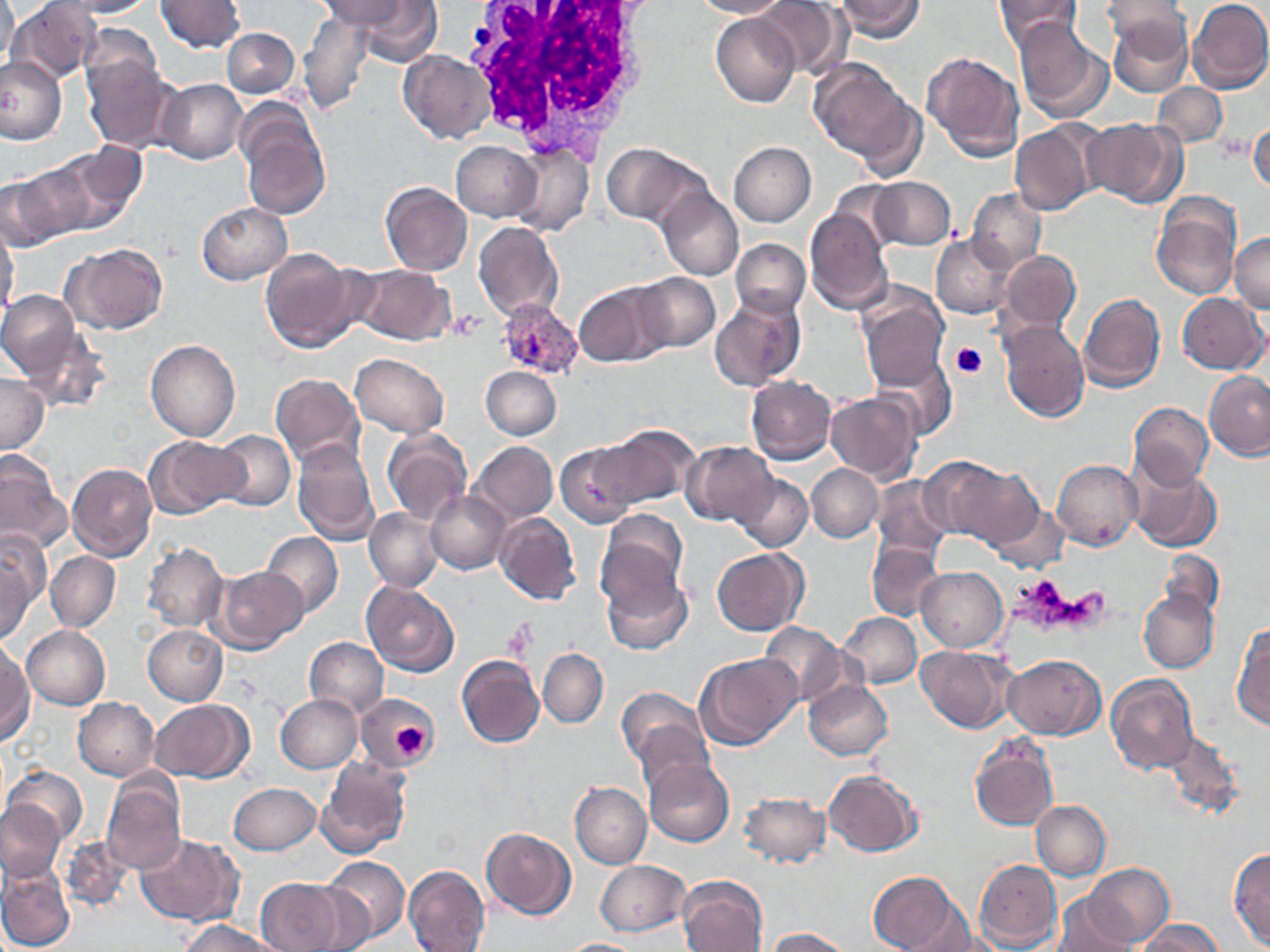

Approximate bounding boxes as named x1/y1/x2/y2 corners in pixels. White blood cell locations: (x1=461, y1=0, x2=660, y2=165). Platelet locations: (x1=448, y1=311, x2=484, y2=341), (x1=952, y1=342, x2=988, y2=379), (x1=504, y1=622, x2=538, y2=661), (x1=393, y1=720, x2=428, y2=758). Uninfected red blood cell locations: (x1=1, y1=0, x2=18, y2=74), (x1=7, y1=0, x2=103, y2=84), (x1=57, y1=0, x2=154, y2=18), (x1=155, y1=0, x2=244, y2=53), (x1=321, y1=0, x2=420, y2=36), (x1=691, y1=0, x2=788, y2=19), (x1=756, y1=0, x2=846, y2=79), (x1=834, y1=0, x2=925, y2=41), (x1=993, y1=0, x2=1083, y2=47), (x1=1186, y1=0, x2=1270, y2=93), (x1=352, y1=1, x2=443, y2=65), (x1=1102, y1=1, x2=1192, y2=54), (x1=297, y1=9, x2=374, y2=117), (x1=711, y1=12, x2=800, y2=107), (x1=1107, y1=15, x2=1192, y2=98), (x1=1012, y1=18, x2=1111, y2=121), (x1=225, y1=21, x2=365, y2=109), (x1=78, y1=23, x2=163, y2=101), (x1=222, y1=27, x2=298, y2=98), (x1=398, y1=49, x2=496, y2=144), (x1=922, y1=51, x2=1024, y2=161), (x1=0, y1=55, x2=66, y2=145), (x1=81, y1=56, x2=175, y2=153), (x1=809, y1=59, x2=914, y2=161), (x1=158, y1=79, x2=247, y2=165), (x1=1153, y1=82, x2=1227, y2=148), (x1=856, y1=99, x2=927, y2=184), (x1=237, y1=105, x2=330, y2=220), (x1=1083, y1=116, x2=1189, y2=208), (x1=1248, y1=116, x2=1270, y2=197), (x1=1009, y1=121, x2=1100, y2=216), (x1=452, y1=141, x2=542, y2=222), (x1=728, y1=142, x2=816, y2=226), (x1=600, y1=143, x2=709, y2=228), (x1=507, y1=144, x2=593, y2=238), (x1=46, y1=146, x2=143, y2=232), (x1=0, y1=172, x2=73, y2=250), (x1=868, y1=177, x2=956, y2=251), (x1=379, y1=182, x2=472, y2=275), (x1=657, y1=188, x2=743, y2=280), (x1=967, y1=188, x2=1046, y2=273), (x1=1151, y1=194, x2=1241, y2=301), (x1=197, y1=202, x2=292, y2=284), (x1=804, y1=207, x2=894, y2=314), (x1=0, y1=219, x2=20, y2=322), (x1=473, y1=223, x2=562, y2=322), (x1=931, y1=232, x2=1016, y2=318), (x1=1230, y1=234, x2=1270, y2=312), (x1=731, y1=239, x2=810, y2=318), (x1=63, y1=241, x2=169, y2=335), (x1=259, y1=247, x2=361, y2=352), (x1=996, y1=250, x2=1081, y2=336), (x1=353, y1=264, x2=455, y2=345), (x1=631, y1=273, x2=720, y2=353), (x1=574, y1=282, x2=667, y2=367), (x1=856, y1=287, x2=949, y2=388), (x1=0, y1=290, x2=80, y2=380), (x1=1077, y1=291, x2=1166, y2=394), (x1=1178, y1=292, x2=1268, y2=375), (x1=709, y1=296, x2=803, y2=392), (x1=997, y1=319, x2=1088, y2=423), (x1=20, y1=328, x2=112, y2=414), (x1=146, y1=340, x2=240, y2=441), (x1=869, y1=353, x2=958, y2=441), (x1=350, y1=354, x2=449, y2=438), (x1=481, y1=367, x2=561, y2=439), (x1=1204, y1=371, x2=1270, y2=461), (x1=0, y1=373, x2=49, y2=455), (x1=270, y1=373, x2=366, y2=469), (x1=745, y1=376, x2=836, y2=464), (x1=824, y1=392, x2=921, y2=484), (x1=1128, y1=403, x2=1213, y2=490), (x1=597, y1=425, x2=700, y2=510), (x1=381, y1=428, x2=473, y2=526), (x1=213, y1=430, x2=295, y2=512), (x1=143, y1=435, x2=249, y2=518), (x1=292, y1=440, x2=380, y2=546), (x1=469, y1=441, x2=558, y2=524), (x1=555, y1=441, x2=641, y2=526), (x1=680, y1=441, x2=778, y2=527), (x1=0, y1=454, x2=67, y2=555), (x1=922, y1=456, x2=1030, y2=546), (x1=1052, y1=459, x2=1143, y2=551), (x1=1126, y1=459, x2=1222, y2=552), (x1=67, y1=462, x2=159, y2=561), (x1=806, y1=464, x2=883, y2=542), (x1=733, y1=473, x2=812, y2=552), (x1=871, y1=476, x2=953, y2=560), (x1=426, y1=492, x2=511, y2=574), (x1=988, y1=503, x2=1068, y2=575), (x1=364, y1=508, x2=443, y2=592), (x1=494, y1=512, x2=582, y2=606), (x1=597, y1=512, x2=688, y2=615), (x1=0, y1=531, x2=49, y2=616), (x1=262, y1=532, x2=342, y2=617), (x1=866, y1=540, x2=944, y2=623), (x1=143, y1=542, x2=227, y2=632), (x1=711, y1=548, x2=807, y2=635), (x1=1156, y1=550, x2=1224, y2=624), (x1=0, y1=551, x2=34, y2=645), (x1=45, y1=551, x2=120, y2=631), (x1=213, y1=565, x2=309, y2=653), (x1=915, y1=566, x2=1007, y2=652), (x1=602, y1=570, x2=692, y2=655), (x1=360, y1=582, x2=460, y2=677), (x1=1139, y1=590, x2=1218, y2=674), (x1=838, y1=612, x2=922, y2=688), (x1=1231, y1=621, x2=1270, y2=731), (x1=758, y1=623, x2=850, y2=707), (x1=144, y1=624, x2=228, y2=704), (x1=22, y1=625, x2=111, y2=710), (x1=304, y1=638, x2=388, y2=717), (x1=916, y1=646, x2=1014, y2=732), (x1=538, y1=648, x2=609, y2=728), (x1=0, y1=650, x2=32, y2=747), (x1=695, y1=652, x2=802, y2=749), (x1=1003, y1=654, x2=1105, y2=739), (x1=456, y1=656, x2=544, y2=750), (x1=1106, y1=674, x2=1196, y2=772), (x1=803, y1=681, x2=893, y2=761), (x1=617, y1=688, x2=709, y2=769), (x1=356, y1=691, x2=438, y2=769), (x1=275, y1=694, x2=363, y2=773), (x1=72, y1=697, x2=160, y2=781), (x1=149, y1=700, x2=253, y2=781), (x1=634, y1=720, x2=715, y2=799), (x1=1161, y1=731, x2=1245, y2=819), (x1=969, y1=738, x2=1057, y2=832), (x1=317, y1=757, x2=411, y2=858), (x1=643, y1=757, x2=733, y2=847), (x1=4, y1=765, x2=87, y2=847), (x1=823, y1=770, x2=921, y2=856), (x1=102, y1=773, x2=186, y2=874), (x1=570, y1=782, x2=652, y2=868), (x1=228, y1=783, x2=321, y2=855), (x1=739, y1=793, x2=830, y2=867), (x1=0, y1=800, x2=65, y2=880), (x1=1031, y1=801, x2=1111, y2=880), (x1=481, y1=826, x2=575, y2=920), (x1=61, y1=835, x2=132, y2=914), (x1=136, y1=835, x2=240, y2=926), (x1=1229, y1=848, x2=1270, y2=948), (x1=322, y1=855, x2=410, y2=943), (x1=972, y1=859, x2=1062, y2=950), (x1=595, y1=860, x2=690, y2=936), (x1=1083, y1=863, x2=1173, y2=946), (x1=403, y1=864, x2=489, y2=951), (x1=0, y1=868, x2=74, y2=951), (x1=868, y1=871, x2=970, y2=952), (x1=676, y1=875, x2=768, y2=952), (x1=254, y1=878, x2=351, y2=952), (x1=1050, y1=893, x2=1139, y2=952), (x1=181, y1=919, x2=277, y2=952), (x1=1136, y1=919, x2=1226, y2=952), (x1=766, y1=927, x2=852, y2=951), (x1=555, y1=938, x2=651, y2=952). Plasmodium vivax-infected red blood cell locations: (x1=497, y1=298, x2=583, y2=379). Slide-level diagnosis: Plasmodium vivax. 1000x magnification. Image is 1270×952 pixels. Single field of view. Thin blood smear. May-Grünwald-Giemsa-stained preparation. Optical microscopy.